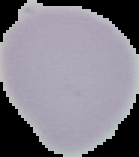
Summary:
  - Image size: 139×157 pixels
  - Image type: segmented cell region on a black background
  - Malaria status: uninfected
  - Preparation: thin blood smear